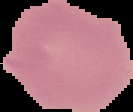
preparation = thin blood smear
malaria status = uninfected
image size = 133×112 pixels
image type = segmented cell region with the area outside set to black